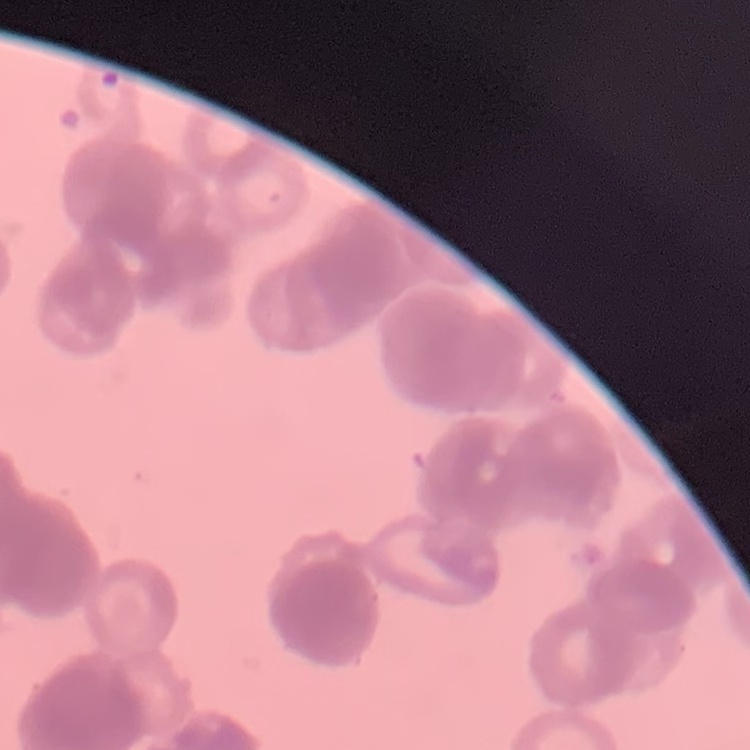
Summary:
  - Erythrocyte morphology: rouleaux formation
  - Stain: Field's or Giemsa
  - Preparation: thin peripheral smear
  - Image type: square crop of a larger photomicrograph